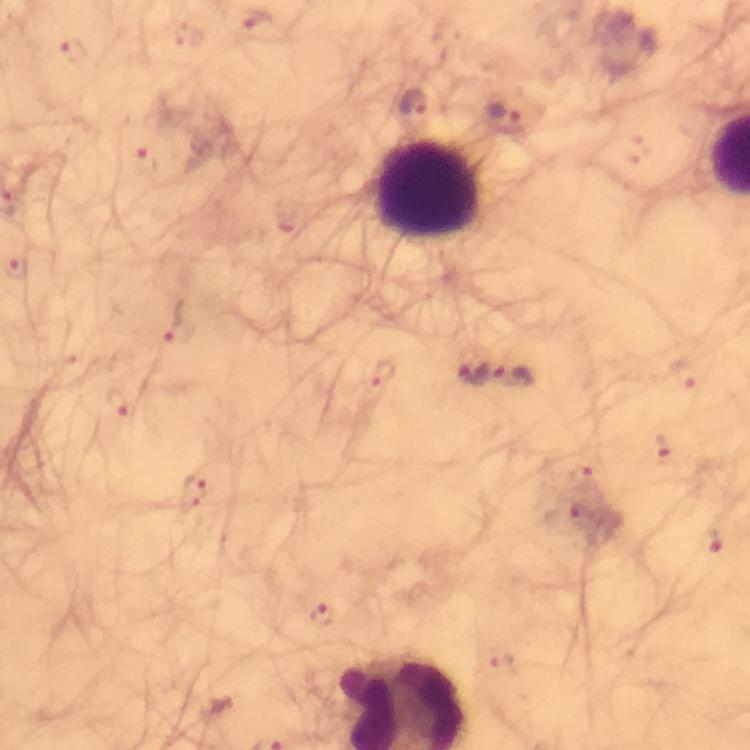

Approximate centers as {x, y} in pixels.
Summary:
  - Leukocyte locations: {426, 188}
  - Plasmodium parasite locations: {257, 21}, {191, 35}, {73, 52}, {412, 102}, {502, 113}, {637, 150}, {146, 161}, {284, 224}, {18, 270}, {175, 320}, {381, 372}, {474, 373}, {682, 375}, {515, 377}, {118, 403}, {663, 448}, {584, 477}, {196, 496}, {564, 518}, {710, 542}, {324, 614}, {501, 664}
  - Stain: Giemsa
  - Preparation: thick smear
  - Context: from a malaria diagnostic workup
  - Magnification: 100x
  - Cropped from: a single field of view
  - Capture: smartphone photograph through a microscope
  - Image size: 750×750 pixels
  - Immersion oil: applied